Outline each blood parasite and name the species.
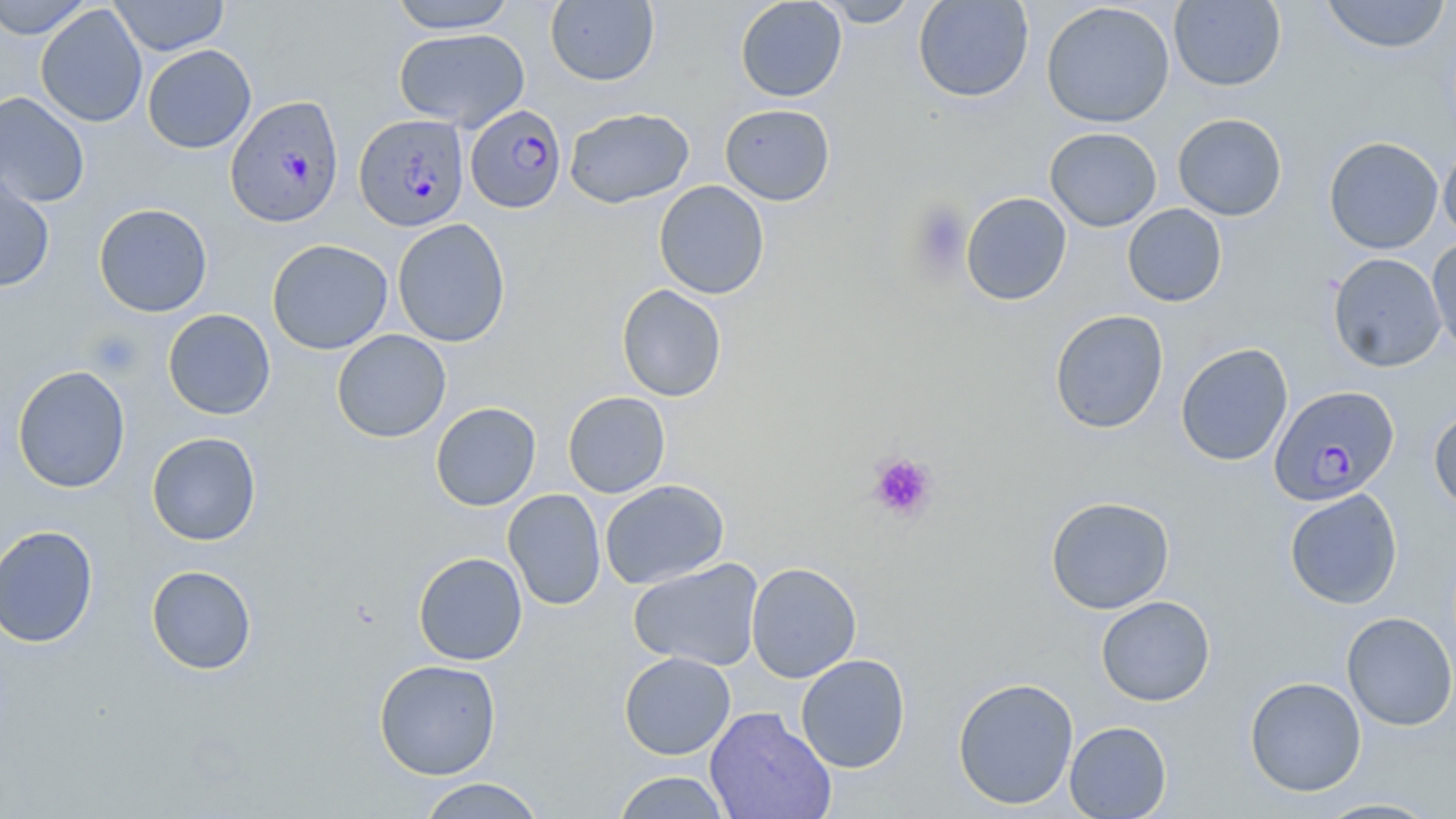
Approximate bounding boxes as (x1, y1, x2, y2) in pixels.
Plasmodium falciparum-infected red blood cells: (225, 95, 345, 228), (465, 104, 567, 214), (354, 113, 469, 232), (1270, 385, 1400, 506).
No Plasmodium ovale, Plasmodium malariae, Plasmodium vivax, Babesia divergens, or Trypanosoma brucei observed.

slide-level diagnosis = Plasmodium falciparum
preparation = thin blood smear
uninfected red blood cell locations = approximate bounding boxes as (x1, y1, x2, y2) in pixels: (0, 0, 93, 39), (110, 0, 230, 56), (388, 0, 518, 33), (735, 0, 847, 102), (815, 0, 920, 27), (913, 0, 1034, 102), (1318, 0, 1452, 54), (545, 1, 659, 87), (1169, 1, 1286, 91), (1041, 2, 1175, 128), (35, 5, 147, 127), (392, 28, 530, 130), (142, 44, 256, 154), (0, 91, 91, 208), (720, 104, 835, 206), (564, 107, 695, 208), (1172, 113, 1288, 221), (1045, 127, 1162, 231), (1323, 136, 1443, 254), (1438, 141, 1456, 244), (0, 169, 55, 293), (653, 180, 770, 299), (961, 192, 1072, 306), (94, 203, 212, 317), (1122, 203, 1227, 307), (392, 218, 511, 347), (1427, 236, 1456, 360), (267, 239, 393, 355), (1327, 252, 1447, 372), (616, 284, 727, 402), (162, 309, 276, 420), (1049, 310, 1169, 434), (332, 329, 451, 443), (1176, 342, 1293, 467), (12, 365, 131, 493), (563, 391, 670, 498), (430, 402, 541, 511), (1428, 404, 1456, 513), (146, 431, 262, 546), (600, 479, 729, 589), (503, 488, 606, 611), (1284, 488, 1403, 609), (1045, 496, 1175, 615), (0, 524, 99, 648), (413, 552, 528, 665), (628, 558, 764, 671), (746, 562, 862, 683), (146, 564, 257, 675), (1096, 596, 1215, 706), (1341, 611, 1456, 731), (619, 651, 736, 760), (795, 654, 910, 772), (374, 659, 501, 780), (1244, 676, 1367, 797), (952, 677, 1079, 809), (704, 706, 836, 819), (1065, 721, 1171, 818), (612, 771, 732, 818), (415, 777, 546, 818), (1310, 797, 1444, 818)
field of view = single
modality = light microscopy
magnification = 1000x
stain = May-Grünwald-Giemsa
image size = 1456×819 pixels
platelet locations = approximate bounding boxes as (x1, y1, x2, y2) in pixels: (907, 200, 972, 276), (86, 329, 144, 378), (867, 451, 939, 522)